Locate every Plasmodium parasite.
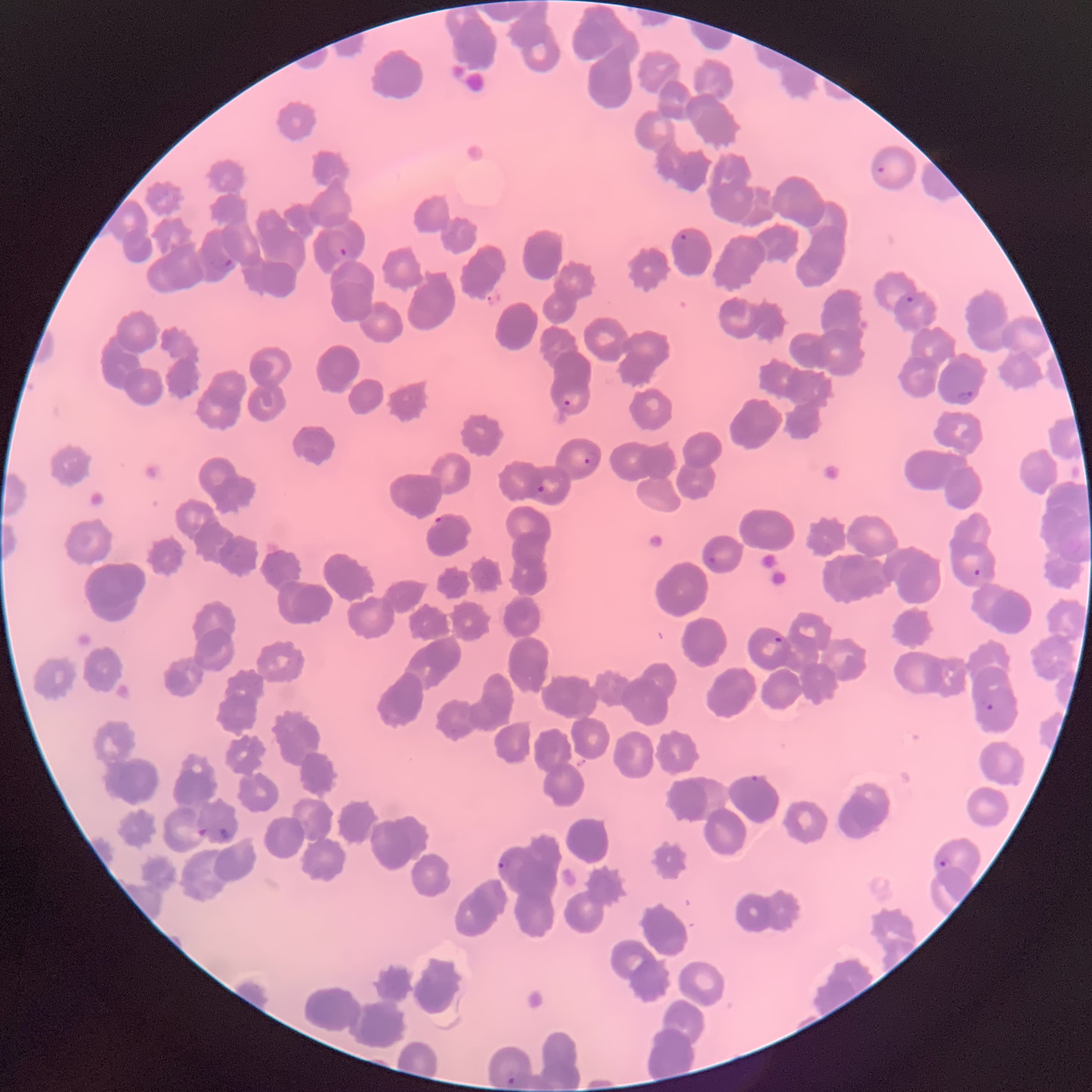
Approximate bounding boxes as (x1,y1)-(x2,y2) corner pairs in pixels.
Plasmodium parasites: (876,164)-(887,175), (679,232)-(688,243), (338,246)-(349,259), (210,256)-(235,274), (905,295)-(915,304), (957,388)-(974,401), (563,398)-(572,408), (583,451)-(601,468), (536,484)-(546,495), (434,514)-(445,525), (705,555)-(718,569), (971,568)-(983,579), (773,636)-(784,646), (982,697)-(995,713), (749,774)-(760,784), (196,827)-(209,838), (212,827)-(231,843), (497,855)-(510,871), (939,856)-(952,870), (506,1074)-(516,1085).

modality = optical microscopy
red blood cell morphology = rouleaux formation
preparation = thin blood film
image size = 1092×1092 pixels